Name the parasite shown.
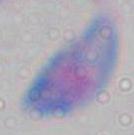
Toxoplasma gondii.

magnification = 1000x
modality = photomicrograph